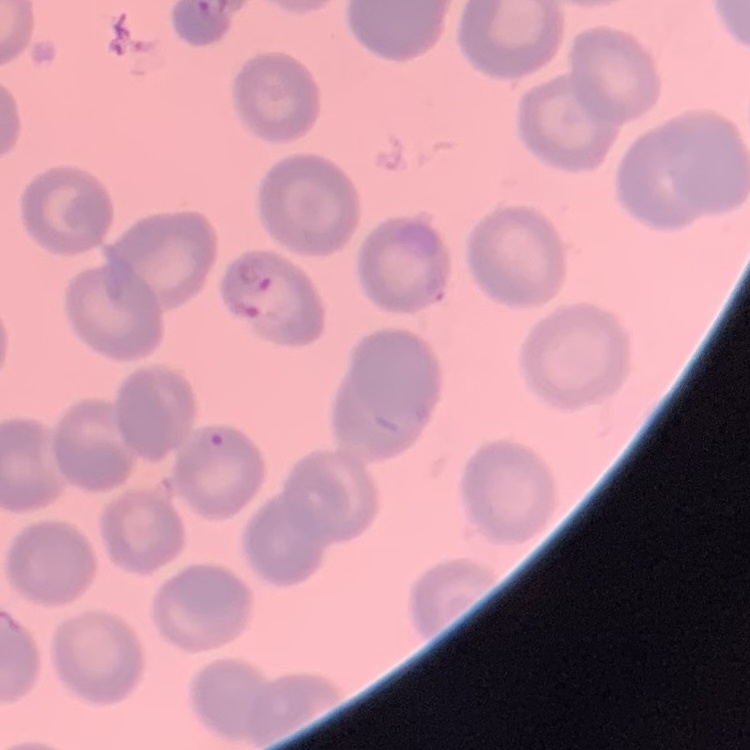
Summary:
  - Red blood cell morphology: no rouleaux formation
  - Preparation: thin blood smear
  - Stain: Field's or Giemsa
  - Image type: square crop of a larger photomicrograph